Report the malaria status of this cell.
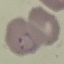
It is parasitized.

Thin blood smear. Giemsa stain. Acquired by smartphone through the microscope eyepiece. Cell patch, automatically extracted from a larger field of view and resized to 64 × 64 pixels.